Identify the preparation type.
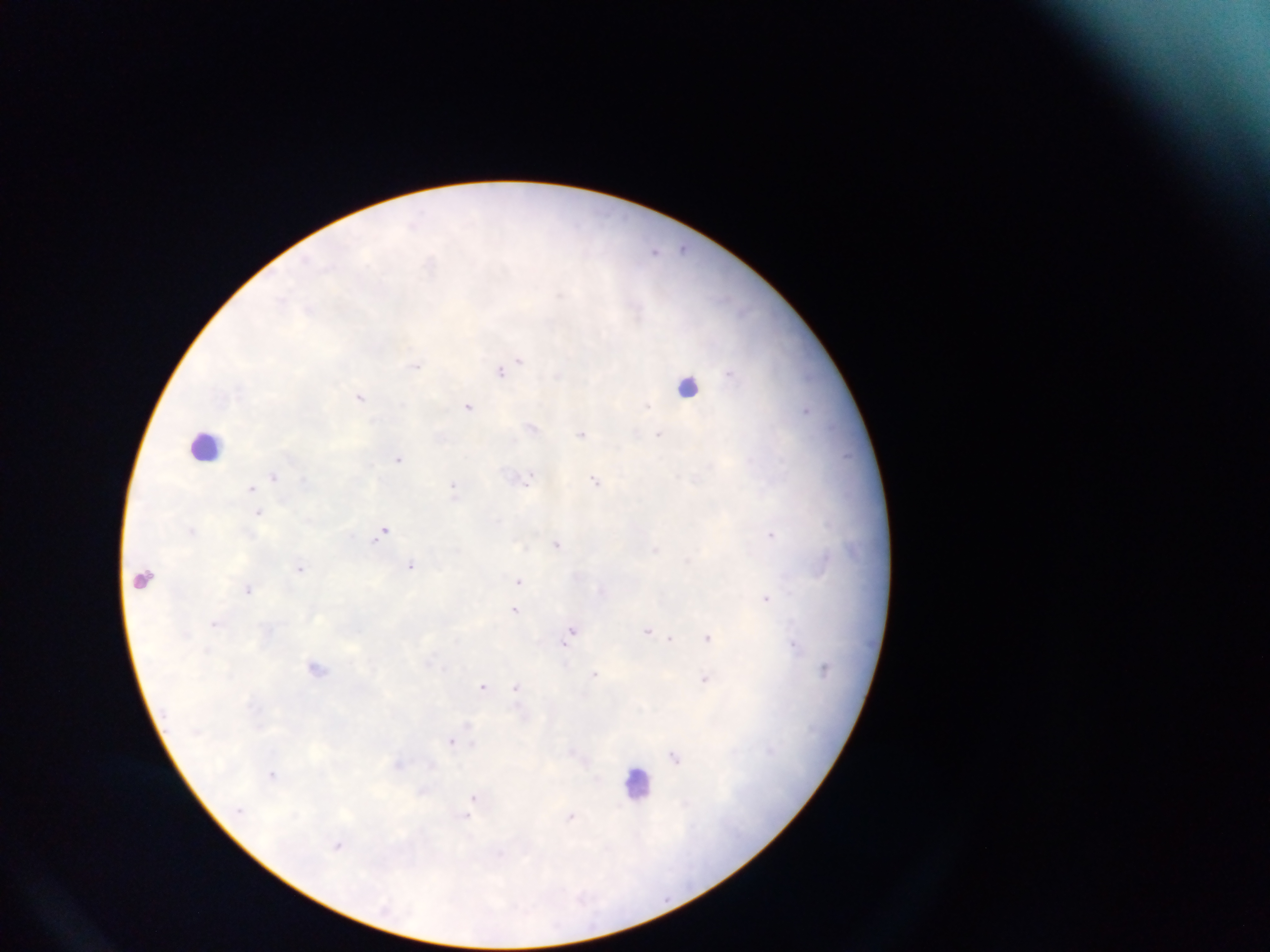

Thick blood smear.

Approximate centers as (x, y) in pixels.
Summary:
  - Malaria parasite locations: (685, 248), (656, 250), (560, 294), (508, 366), (417, 367), (359, 396), (468, 406), (533, 427), (657, 433), (582, 435), (849, 455), (400, 459), (531, 477), (596, 479), (256, 485), (453, 488), (192, 531), (384, 531), (771, 534), (557, 544), (655, 550), (687, 560), (411, 565), (300, 567), (519, 581), (248, 591), (766, 597), (516, 609), (214, 623), (573, 629), (648, 630), (671, 638), (709, 638), (800, 644), (208, 648), (568, 649), (314, 665), (595, 672), (702, 679), (484, 685), (516, 686), (468, 724), (452, 740), (676, 758), (431, 764), (399, 765), (273, 772), (473, 800), (572, 817), (339, 845)
  - Leukocyte locations: (686, 384), (204, 447), (141, 579)
  - Field of view: single
  - Image size: 1270×952 pixels
  - Country: Ghana
  - Capture: mobile-phone photograph through a microscope